Identify the blood parasite species.
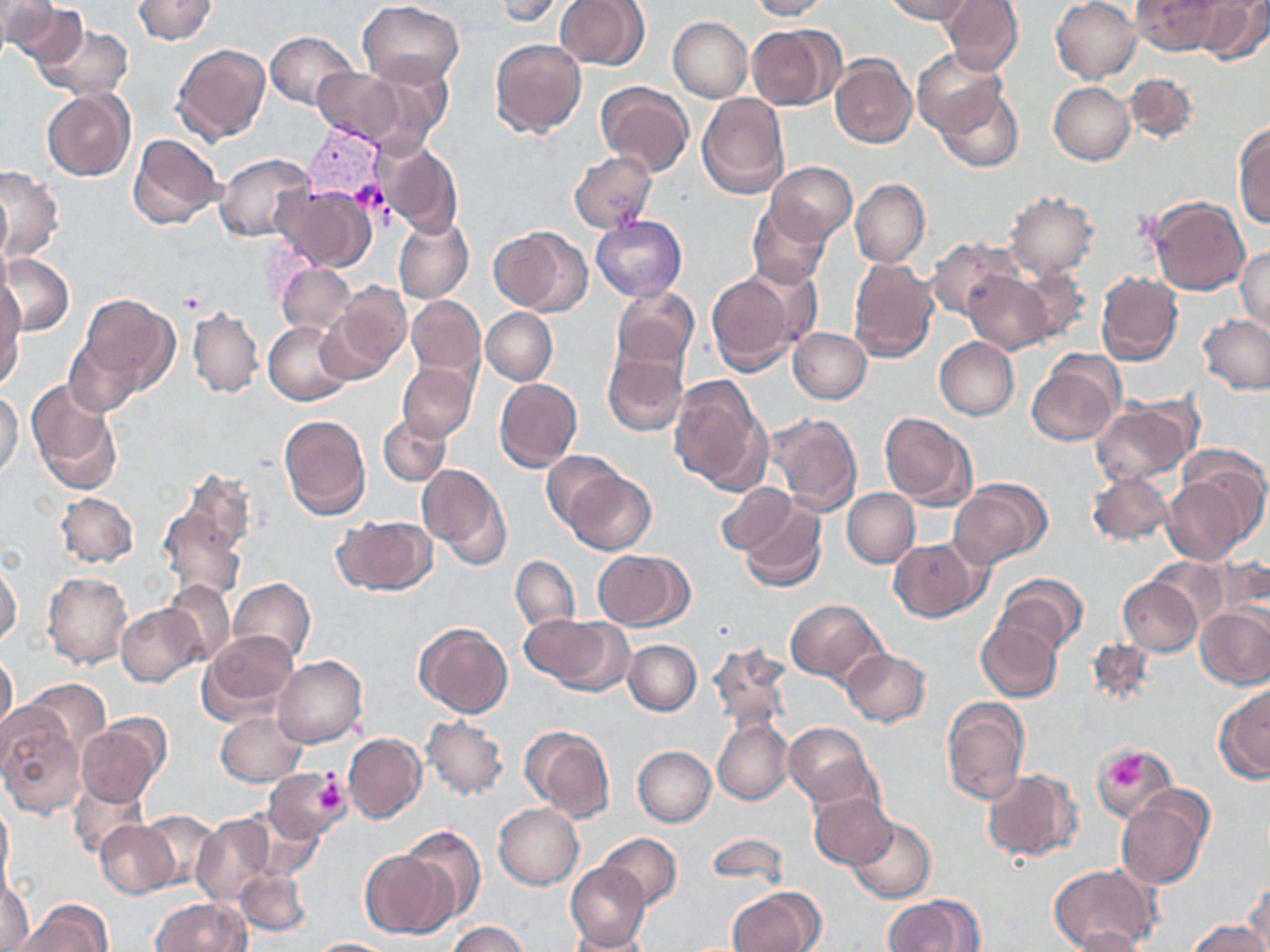
Plasmodium vivax.

platelet_locations: 'approximate bounding boxes as named x1/y1/x2/y2 corners in pixels: (x1=1109, y1=748, x2=1148, y2=789), (x1=312, y1=772, x2=348, y2=820)'
stain: May-Grünwald-Giemsa
plasmodium_vivax_infected_red_blood_cell_locations: 'approximate bounding boxes as named x1/y1/x2/y2 corners in pixels: (x1=303, y1=122, x2=387, y2=208)'
field_of_view: single
preparation: thin blood film
image_size: 1270×952 pixels
uninfected_red_blood_cell_locations: 'approximate bounding boxes as named x1/y1/x2/y2 corners in pixels: (x1=133, y1=0, x2=216, y2=45), (x1=493, y1=0, x2=568, y2=24), (x1=746, y1=0, x2=833, y2=20), (x1=881, y1=0, x2=974, y2=23), (x1=940, y1=0, x2=1023, y2=75), (x1=1051, y1=0, x2=1142, y2=84), (x1=1132, y1=0, x2=1225, y2=56), (x1=1191, y1=0, x2=1268, y2=64), (x1=3, y1=1, x2=86, y2=70), (x1=553, y1=1, x2=651, y2=71), (x1=357, y1=2, x2=465, y2=87), (x1=667, y1=17, x2=751, y2=102), (x1=35, y1=22, x2=133, y2=101), (x1=746, y1=23, x2=841, y2=111), (x1=264, y1=31, x2=358, y2=109), (x1=489, y1=39, x2=587, y2=140), (x1=172, y1=43, x2=272, y2=144), (x1=912, y1=48, x2=1008, y2=137), (x1=830, y1=55, x2=917, y2=148), (x1=354, y1=59, x2=457, y2=150), (x1=312, y1=66, x2=413, y2=149), (x1=1124, y1=72, x2=1197, y2=145), (x1=1050, y1=82, x2=1134, y2=165), (x1=595, y1=83, x2=694, y2=178), (x1=936, y1=87, x2=1025, y2=172), (x1=42, y1=89, x2=136, y2=181), (x1=695, y1=93, x2=789, y2=199), (x1=1232, y1=121, x2=1270, y2=227), (x1=128, y1=133, x2=225, y2=229), (x1=376, y1=141, x2=464, y2=238), (x1=215, y1=152, x2=314, y2=242), (x1=568, y1=152, x2=657, y2=233), (x1=766, y1=162, x2=856, y2=244), (x1=0, y1=166, x2=62, y2=260), (x1=851, y1=179, x2=930, y2=268), (x1=1, y1=181, x2=12, y2=264), (x1=274, y1=183, x2=376, y2=273), (x1=1006, y1=191, x2=1097, y2=278), (x1=1147, y1=196, x2=1250, y2=296), (x1=747, y1=201, x2=831, y2=288), (x1=590, y1=215, x2=686, y2=301), (x1=393, y1=216, x2=473, y2=303), (x1=490, y1=226, x2=592, y2=317), (x1=925, y1=238, x2=1017, y2=319), (x1=1235, y1=246, x2=1270, y2=334), (x1=2, y1=254, x2=74, y2=336), (x1=848, y1=258, x2=939, y2=362), (x1=277, y1=262, x2=354, y2=334), (x1=1011, y1=267, x2=1092, y2=346), (x1=705, y1=270, x2=805, y2=375), (x1=963, y1=270, x2=1054, y2=354), (x1=1096, y1=272, x2=1182, y2=367), (x1=329, y1=282, x2=410, y2=374), (x1=1, y1=286, x2=25, y2=387), (x1=609, y1=286, x2=699, y2=379), (x1=80, y1=294, x2=178, y2=394), (x1=406, y1=295, x2=484, y2=388), (x1=187, y1=306, x2=264, y2=399), (x1=481, y1=307, x2=557, y2=385), (x1=1198, y1=314, x2=1270, y2=393), (x1=263, y1=320, x2=355, y2=406), (x1=788, y1=327, x2=871, y2=404), (x1=65, y1=336, x2=143, y2=417), (x1=934, y1=337, x2=1019, y2=420), (x1=602, y1=348, x2=687, y2=436), (x1=1026, y1=358, x2=1122, y2=447), (x1=398, y1=362, x2=478, y2=441), (x1=668, y1=374, x2=774, y2=496), (x1=494, y1=378, x2=582, y2=472), (x1=25, y1=380, x2=122, y2=495), (x1=0, y1=391, x2=23, y2=477), (x1=1090, y1=396, x2=1201, y2=485), (x1=767, y1=411, x2=862, y2=516), (x1=880, y1=412, x2=976, y2=509), (x1=278, y1=414, x2=371, y2=520), (x1=379, y1=414, x2=451, y2=485), (x1=542, y1=450, x2=623, y2=529), (x1=417, y1=462, x2=512, y2=568), (x1=171, y1=467, x2=259, y2=567), (x1=565, y1=470, x2=656, y2=555), (x1=1086, y1=471, x2=1174, y2=546), (x1=1162, y1=472, x2=1257, y2=565), (x1=951, y1=479, x2=1049, y2=567), (x1=715, y1=482, x2=800, y2=556), (x1=843, y1=488, x2=919, y2=567), (x1=55, y1=492, x2=138, y2=568), (x1=157, y1=499, x2=248, y2=602), (x1=738, y1=500, x2=826, y2=593), (x1=332, y1=515, x2=436, y2=597), (x1=889, y1=538, x2=985, y2=621), (x1=594, y1=551, x2=692, y2=630), (x1=511, y1=556, x2=579, y2=634), (x1=1146, y1=558, x2=1231, y2=630), (x1=0, y1=563, x2=22, y2=647), (x1=43, y1=571, x2=132, y2=669), (x1=995, y1=572, x2=1088, y2=655), (x1=228, y1=577, x2=314, y2=664), (x1=1119, y1=577, x2=1204, y2=656), (x1=162, y1=580, x2=235, y2=665), (x1=784, y1=599, x2=885, y2=684), (x1=117, y1=604, x2=207, y2=687), (x1=1196, y1=604, x2=1270, y2=689), (x1=529, y1=615, x2=632, y2=695), (x1=977, y1=620, x2=1063, y2=701), (x1=414, y1=622, x2=513, y2=717), (x1=198, y1=630, x2=300, y2=723), (x1=623, y1=640, x2=701, y2=715), (x1=708, y1=640, x2=792, y2=732), (x1=1088, y1=641, x2=1156, y2=707), (x1=841, y1=649, x2=930, y2=727), (x1=0, y1=651, x2=17, y2=742), (x1=273, y1=655, x2=367, y2=748), (x1=20, y1=678, x2=111, y2=760), (x1=1215, y1=685, x2=1270, y2=781), (x1=941, y1=696, x2=1029, y2=805), (x1=0, y1=704, x2=83, y2=818), (x1=215, y1=713, x2=306, y2=785), (x1=422, y1=716, x2=509, y2=800), (x1=75, y1=717, x2=168, y2=811), (x1=713, y1=719, x2=794, y2=806), (x1=519, y1=724, x2=616, y2=821), (x1=785, y1=724, x2=878, y2=807), (x1=347, y1=726, x2=507, y2=811), (x1=343, y1=733, x2=427, y2=823), (x1=1089, y1=742, x2=1177, y2=824), (x1=632, y1=746, x2=716, y2=826), (x1=263, y1=767, x2=350, y2=845), (x1=982, y1=768, x2=1082, y2=862), (x1=69, y1=776, x2=149, y2=860), (x1=808, y1=792, x2=897, y2=869), (x1=1115, y1=793, x2=1212, y2=888), (x1=0, y1=799, x2=13, y2=887), (x1=493, y1=803, x2=584, y2=889), (x1=135, y1=811, x2=222, y2=890), (x1=244, y1=812, x2=322, y2=881), (x1=191, y1=813, x2=276, y2=905), (x1=847, y1=817, x2=936, y2=903), (x1=95, y1=821, x2=180, y2=897), (x1=398, y1=825, x2=486, y2=925), (x1=598, y1=833, x2=681, y2=910), (x1=706, y1=834, x2=789, y2=887), (x1=359, y1=850, x2=454, y2=937), (x1=566, y1=862, x2=649, y2=951), (x1=1048, y1=865, x2=1161, y2=952), (x1=234, y1=866, x2=311, y2=937), (x1=0, y1=871, x2=34, y2=949), (x1=1244, y1=878, x2=1270, y2=951), (x1=728, y1=887, x2=824, y2=952), (x1=885, y1=893, x2=982, y2=952), (x1=152, y1=897, x2=249, y2=951), (x1=14, y1=900, x2=113, y2=951), (x1=1188, y1=920, x2=1266, y2=952), (x1=448, y1=921, x2=529, y2=952), (x1=1063, y1=927, x2=1146, y2=952), (x1=565, y1=930, x2=656, y2=951), (x1=307, y1=937, x2=393, y2=951)'
magnification: 1000x
modality: light microscopy